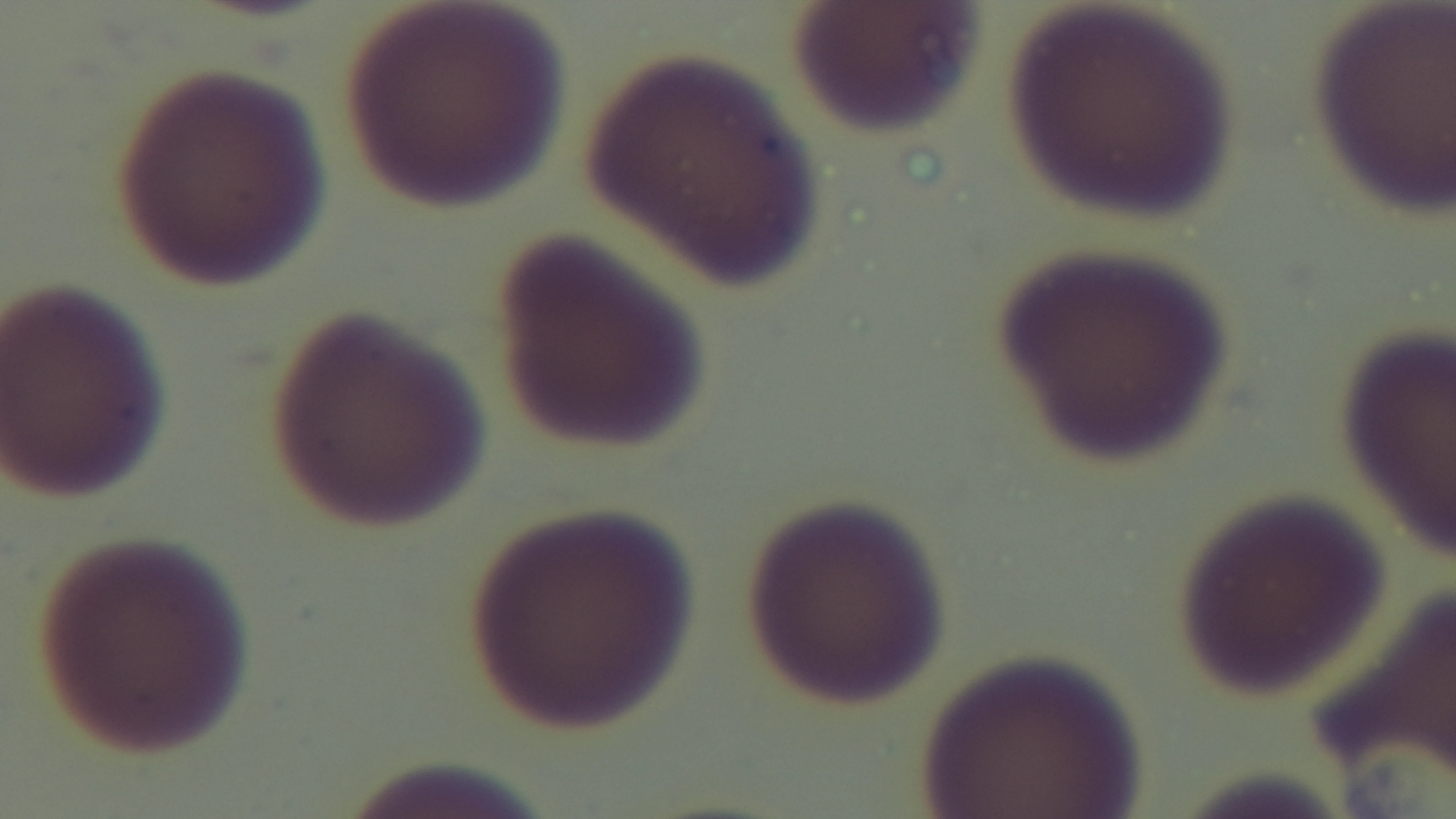

{
  "field_of_view": "single",
  "stain": "Giemsa",
  "preparation": "thin blood film",
  "malaria_status": "negative",
  "capture": "mounted 4K digital camera",
  "objective": "100x oil immersion",
  "modality": "light microscopy"
}